Report the malaria status of this cell.
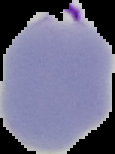

It is parasitized.

{
  "image_size": "115×154 pixels",
  "preparation": "thin blood film",
  "image_type": "segmented cell region with the area outside set to black"
}